Comment on the morphology of the erythrocytes.
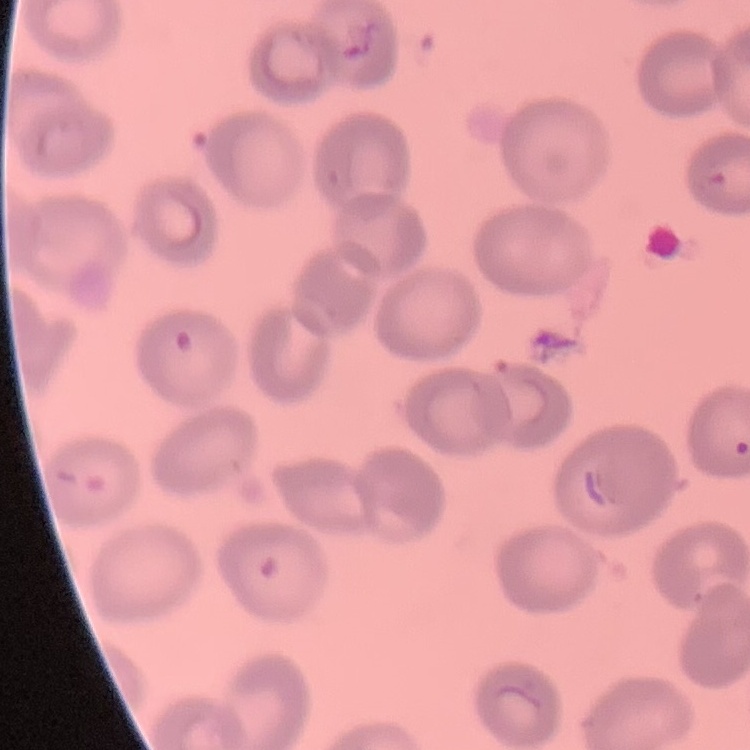

They show no rouleaux formation.

Stained with either Field's or Giemsa. Square crop of a larger photomicrograph. Thin blood smear.